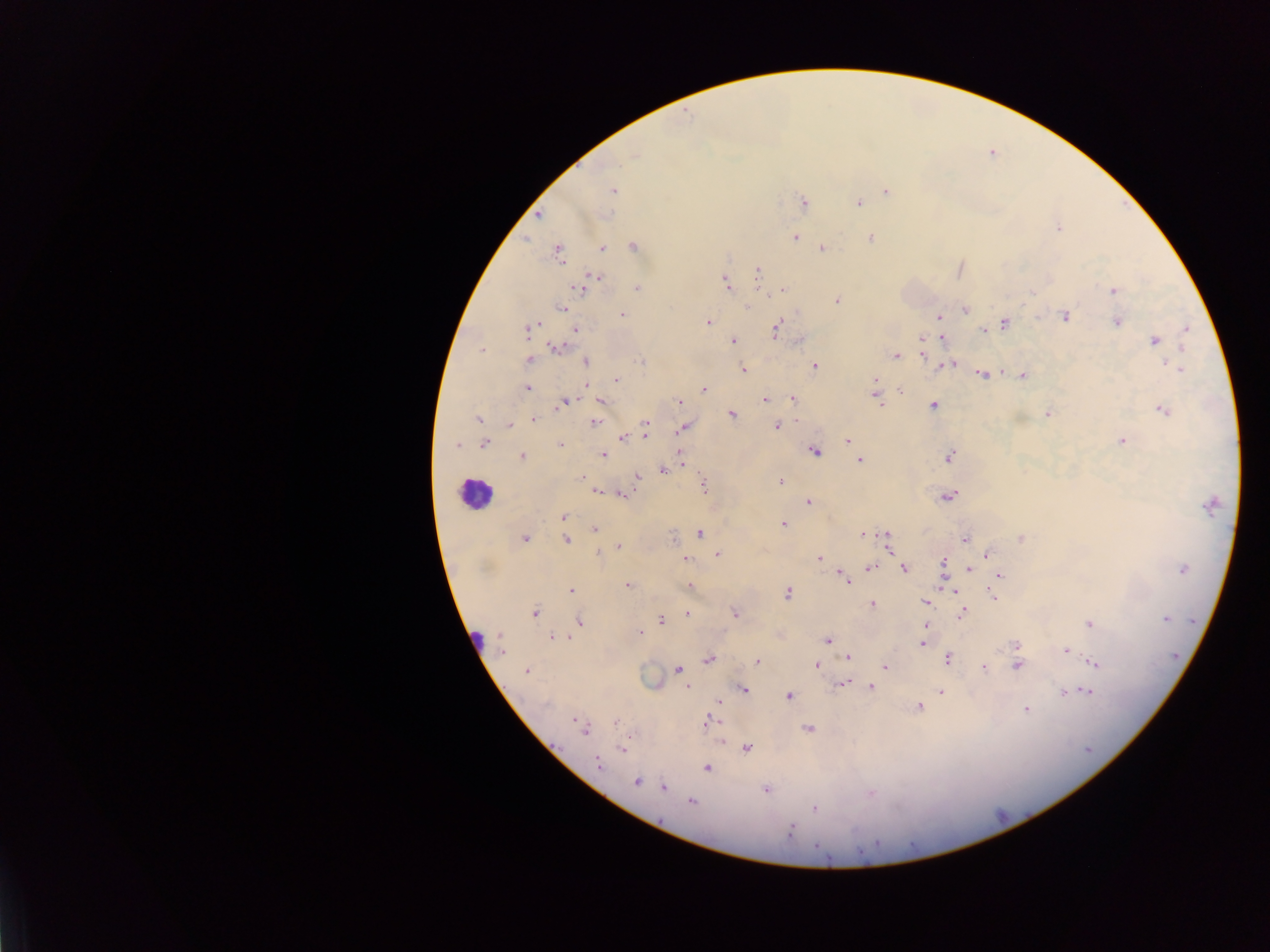

field of view = single
malaria parasite locations = approximate centers as {x, y} in pixels: {634, 155}, {613, 191}, {885, 191}, {803, 201}, {859, 202}, {539, 217}, {1058, 228}, {796, 238}, {869, 239}, {602, 249}, {822, 249}, {558, 251}, {757, 272}, {594, 275}, {726, 283}, {579, 289}, {636, 289}, {783, 290}, {1113, 291}, {836, 298}, {749, 305}, {564, 307}, {965, 311}, {623, 313}, {939, 317}, {1066, 317}, {1116, 323}, {707, 324}, {999, 326}, {775, 328}, {576, 329}, {1185, 329}, {526, 330}, {983, 331}, {942, 337}, {923, 338}, {734, 341}, {1181, 344}, {556, 349}, {922, 354}, {895, 355}, {585, 359}, {529, 361}, {1166, 361}, {640, 362}, {955, 364}, {815, 365}, {741, 369}, {1180, 369}, {983, 375}, {1022, 375}, {875, 378}, {616, 379}, {529, 389}, {704, 390}, {874, 392}, {901, 392}, {793, 399}, {878, 400}, {562, 401}, {571, 401}, {600, 401}, {678, 401}, {766, 401}, {932, 405}, {881, 406}, {1164, 410}, {1047, 414}, {732, 415}, {480, 419}, {534, 419}, {592, 423}, {777, 425}, {511, 426}, {645, 426}, {683, 428}, {646, 434}, {846, 438}, {623, 439}, {1121, 439}, {488, 441}, {484, 443}, {456, 445}, {560, 445}, {680, 451}, {816, 453}, {521, 455}, {604, 455}, {948, 458}, {861, 459}, {684, 464}, {662, 471}, {580, 477}, {638, 477}, {781, 480}, {702, 484}, {597, 491}, {622, 493}, {948, 497}, {807, 502}, {562, 517}, {783, 524}, {594, 528}, {671, 533}, {702, 534}, {886, 534}, {526, 536}, {862, 536}, {1020, 537}, {964, 538}, {565, 541}, {618, 545}, {887, 549}, {598, 551}, {718, 552}, {987, 556}, {820, 557}, {687, 559}, {942, 560}, {871, 568}, {903, 569}, {971, 569}, {1182, 569}, {999, 576}, {848, 582}, {688, 583}, {628, 584}, {954, 590}, {571, 591}, {788, 593}, {993, 596}, {925, 603}, {872, 605}, {963, 612}, {535, 613}, {734, 613}, {687, 614}, {580, 619}, {1165, 620}, {661, 621}, {1088, 624}, {924, 625}, {640, 631}, {499, 636}, {551, 636}, {560, 636}, {569, 638}, {828, 640}, {1017, 645}, {923, 646}, {501, 652}, {1067, 652}, {846, 657}, {948, 657}, {710, 660}, {756, 661}, {1096, 663}, {815, 665}, {1019, 665}, {884, 668}, {678, 669}, {984, 669}, {528, 672}, {840, 686}, {686, 687}, {743, 687}, {870, 687}, {746, 691}, {1087, 692}, {940, 693}, {1062, 694}, {789, 696}, {719, 702}, {544, 705}, {919, 707}, {1025, 709}, {575, 720}, {707, 720}, {615, 722}, {807, 727}, {585, 734}, {720, 742}, {747, 749}, {620, 751}, {596, 764}, {706, 768}, {637, 783}, {662, 787}, {766, 791}, {691, 803}, {813, 808}, {789, 831}, {817, 846}
preparation = thick blood film
country = Ghana
capture = mobile-phone photograph through a microscope
image size = 1270×952 pixels
leukocyte locations = approximate centers as {x, y} in pixels: {472, 491}